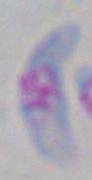 Photomicrograph. Toxoplasma gondii is shown. 1000x magnification.